Report the malaria status.
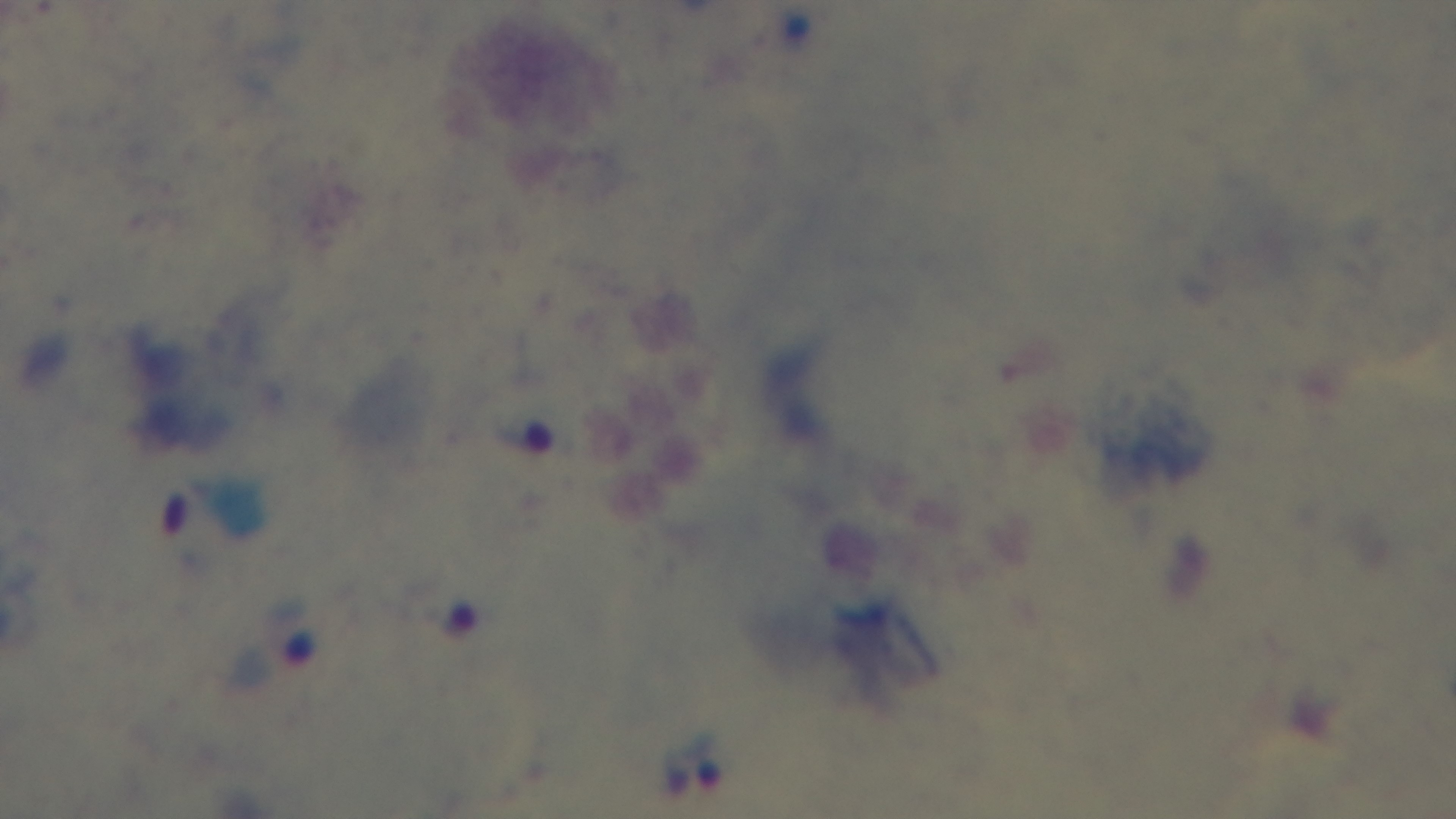

Infected.

100x oil-immersion objective. Preparation: thick blood film. Light microscopy. Single field of view. Captured with a mounted 4K digital camera. Giemsa stain.